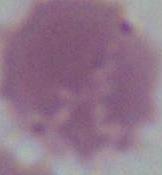

Summary:
  - Identification: red blood cell
  - Magnification: 1000x
  - Modality: photomicrograph